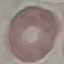

Result: no malaria parasites seen. Thin blood film. Giemsa-stained preparation. Acquired by smartphone through the microscope eyepiece. Automatically extracted cell patch, resized to 64 × 64 pixels.